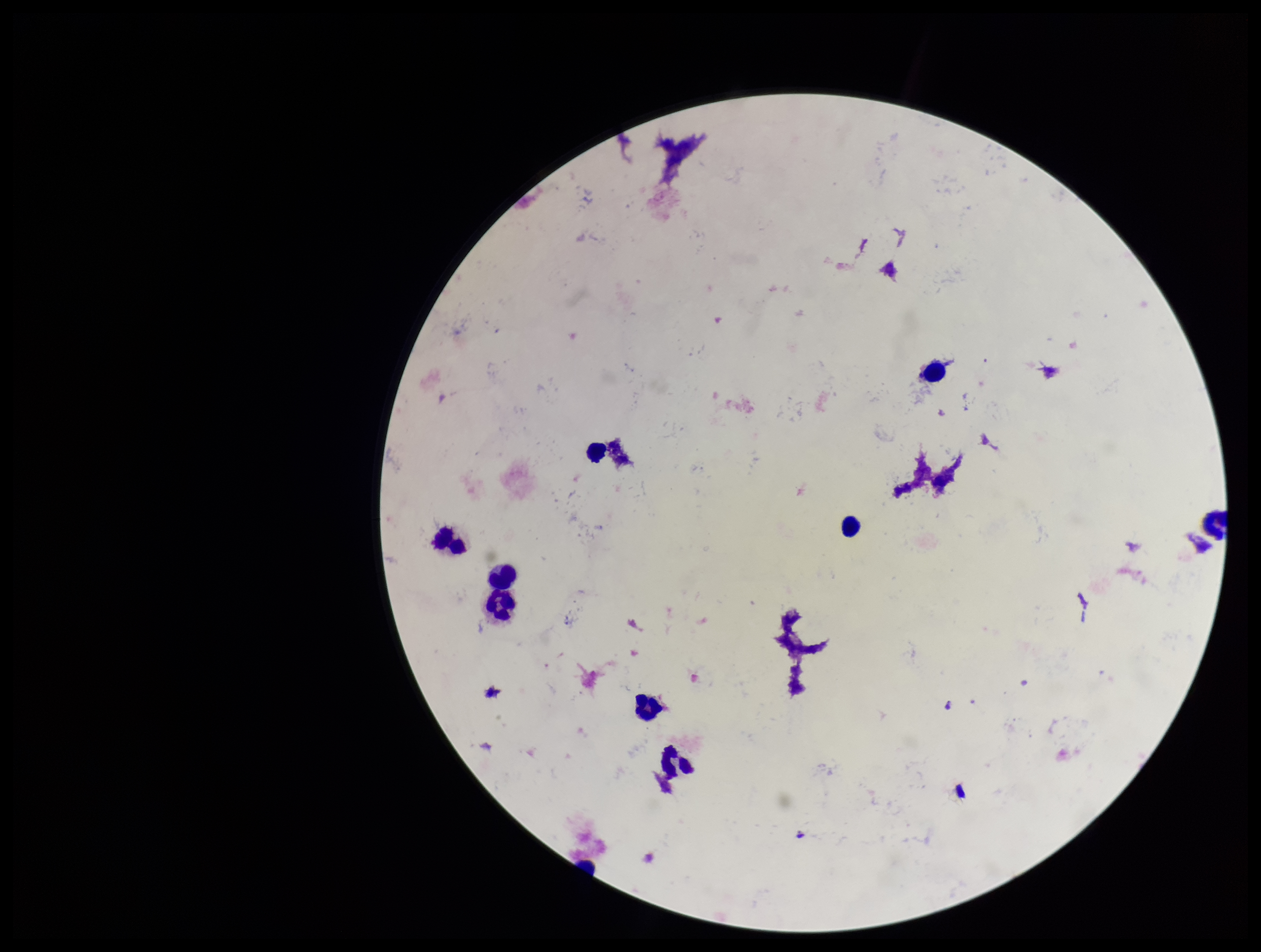

Plasmodium parasites: none identified. Patient malaria status: negative. Image is 1261×952 pixels. Stained with Giemsa. Preparation: thick blood smear. Parasite count: 0. Leukocyte count: 9. One field from this slide. Smartphone photograph taken through the eyepiece of a microscope.